Assess the morphology of the erythrocytes.
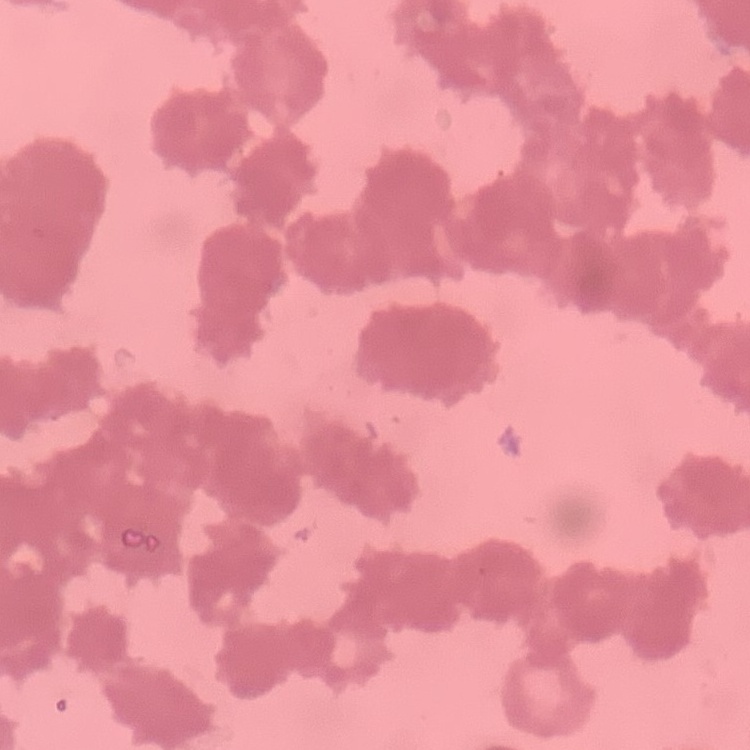

Rouleaux formation.

Summary:
  - Stain: Field's or Giemsa
  - Preparation: thin blood smear
  - Image type: square crop of a larger photomicrograph